Point out each malaria parasite.
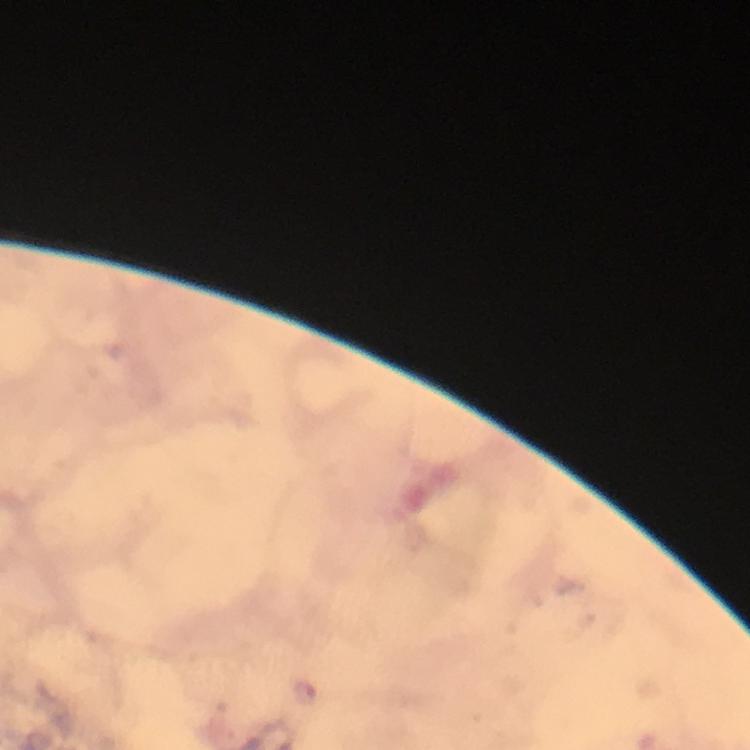
Approximate centers as [x, y] in pixels.
Malaria parasites: [304, 693].

Summary:
  - Immersion oil: used
  - Preparation: thick blood smear
  - Cropped from: a single field of view
  - Capture: smartphone photograph through a microscope
  - Magnification: 100x
  - Stain: Giemsa
  - Image size: 750×750 pixels
  - Context: from a malaria diagnostic workup